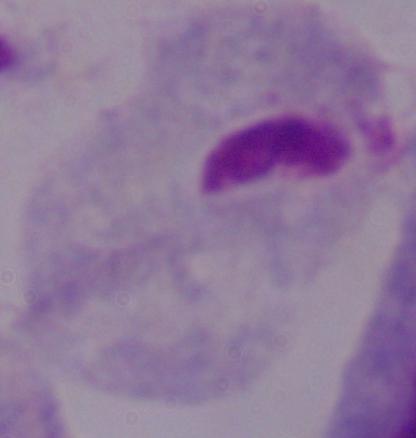 A trichomonad is seen. Micrograph. Captured at 1000x magnification.